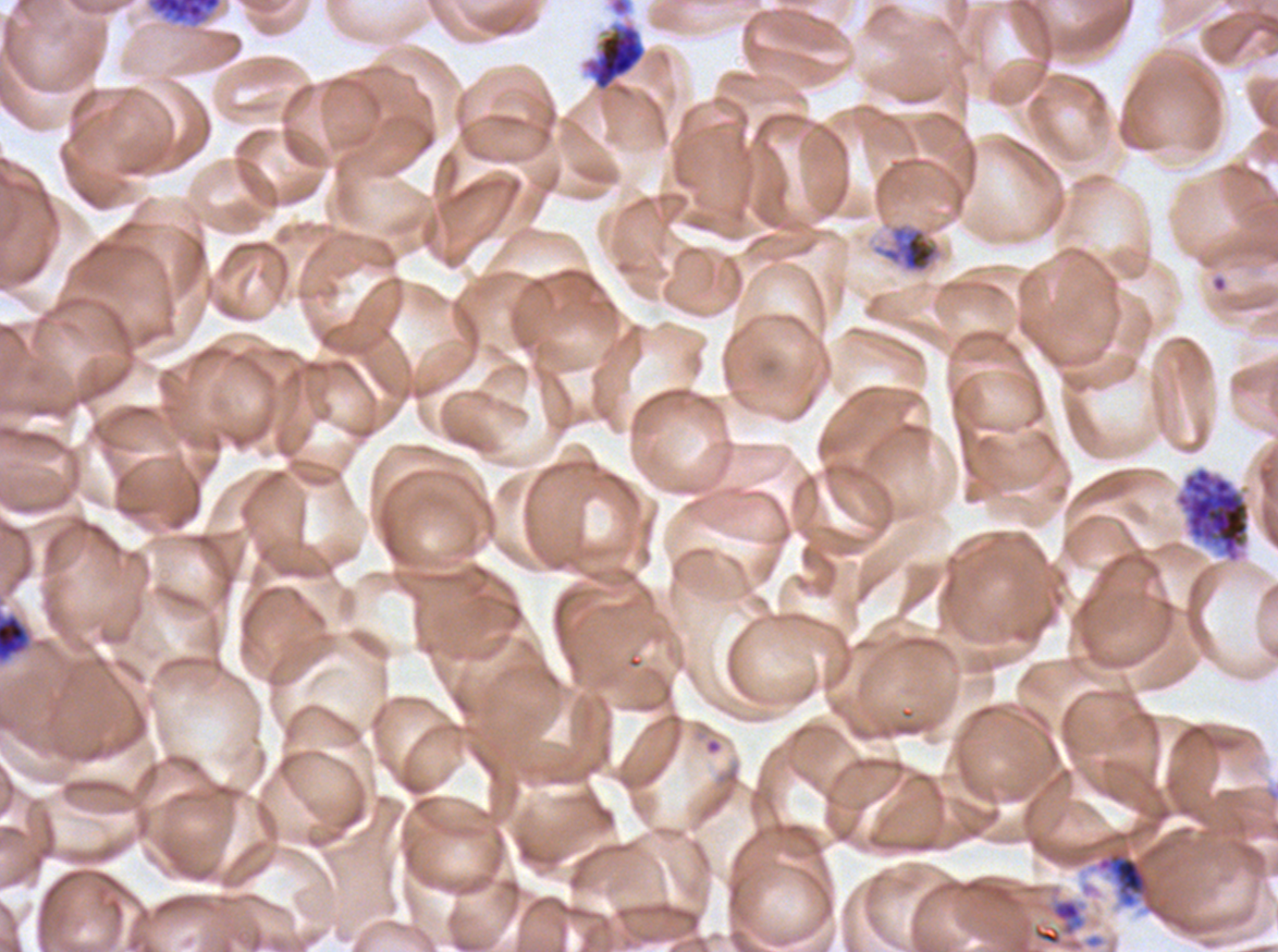

{
  "early_schizont_locations": "approximate bounding rectangles given as corner coordinates in pixels from the top-left: (x1=582, y1=21, x2=646, y2=92), (x1=0, y1=614, x2=29, y2=662)",
  "life_cycle_stages_observed": "late trophozoite, early schizont, late schizont, segmenter",
  "preparation": "thin blood smear",
  "field_of_view": "one sub-image of a larger composite",
  "segmenter_locations": "approximate bounding rectangles given as corner coordinates in pixels from the top-left: (x1=1174, y1=466, x2=1251, y2=564), (x1=1096, y1=849, x2=1153, y2=908)",
  "late_schizont_locations": "approximate bounding rectangles given as corner coordinates in pixels from the top-left: (x1=145, y1=0, x2=223, y2=28)",
  "late_trophozoite_locations": "approximate bounding rectangles given as corner coordinates in pixels from the top-left: (x1=870, y1=221, x2=944, y2=275)",
  "image_size": "1278×952 pixels",
  "stain": "Giemsa",
  "specimen": "ex-vivo P. falciparum culture from a patient in The Gambia, grown for 24 to 48 hours"
}